Identify the cell.
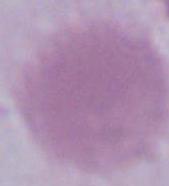
An erythrocyte.

Captured at 1000x magnification. Photomicrograph.